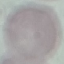

Result: no malaria parasites seen. Cell patch, automatically extracted from a larger field of view and resized to 64 × 64 pixels. Photographed with a smartphone camera at the microscope eyepiece. Giemsa stain. Thin smear of blood.